Identify the parasite.
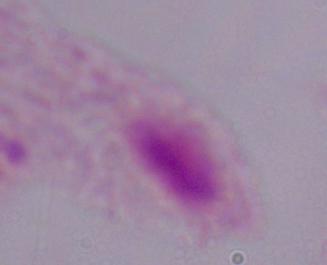

A trichomonad.

1000x magnification. Photomicrograph.